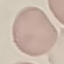 Result: no malaria parasites seen. Cell patch, automatically extracted from a larger field of view and resized to 64 × 64 pixels. Acquired by smartphone through the microscope eyepiece. Giemsa-stained preparation. Thin blood film.